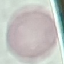

Malaria status: uninfected. Thin smear of blood. Giemsa-stained preparation. Automatically extracted cell patch, resized to 64 × 64 pixels. Photographed with a smartphone camera at the microscope eyepiece.